Describe the morphology of the red blood cells.
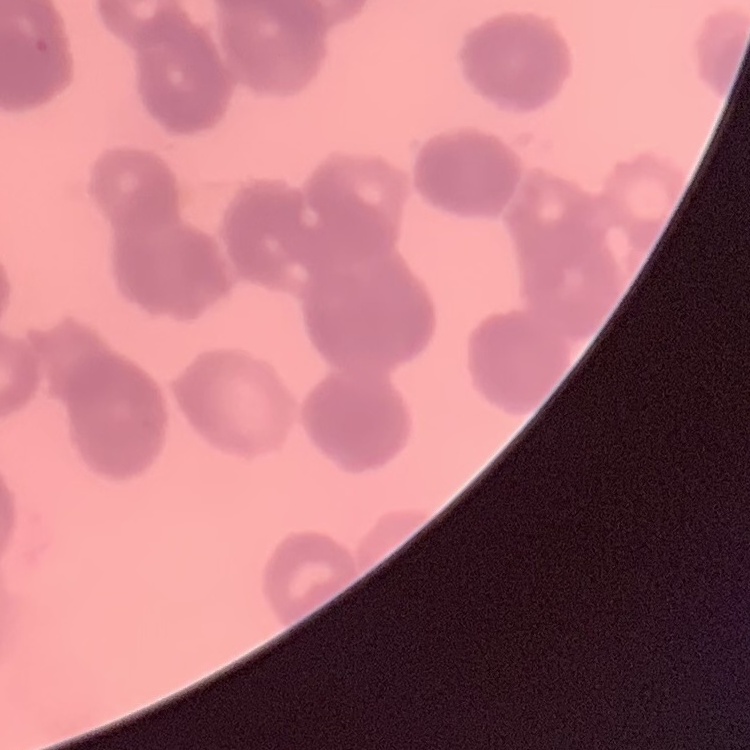
Rouleaux formation.

Thin blood smear. Stained with either Field's or Giemsa. One tile cut from a larger photomicrograph.